Assess this cell for malaria.
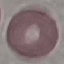
Uninfected.

capture = smartphone through the microscope eyepiece
image type = cell patch, automatically extracted from a larger field of view and resized to 64 × 64 pixels
preparation = thin blood smear
stain = Giemsa